Assess this cell for malaria.
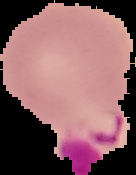
Parasitized.

Summary:
  - Image type: segmented cell region with the area outside set to black
  - Image size: 136×175 pixels
  - Preparation: thin blood film